Locate every leukocyte (white blood cell).
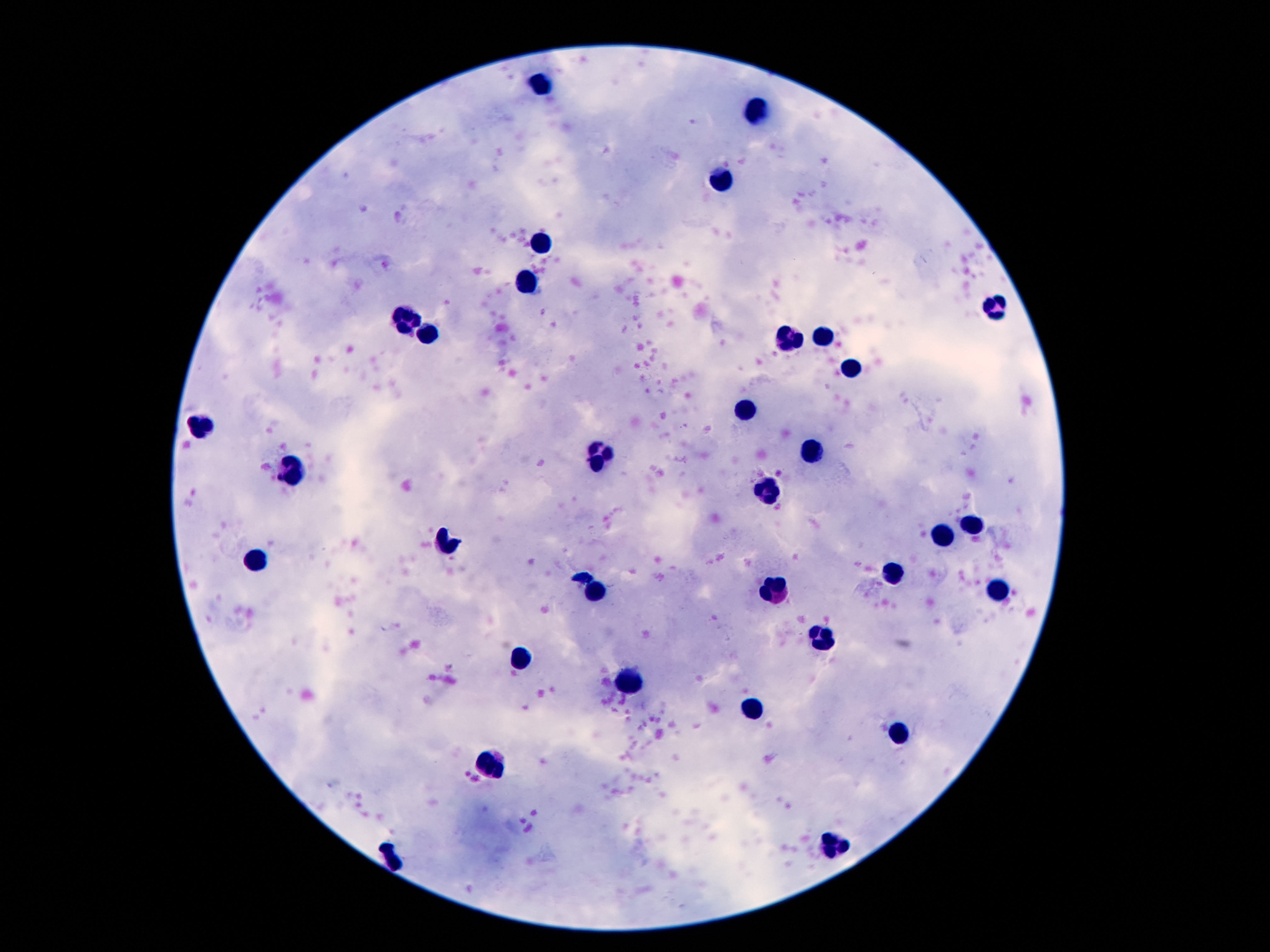

Approximate centers as {x, y} in pixels.
Leukocytes: {541, 82}, {758, 104}, {725, 175}, {539, 242}, {530, 283}, {993, 307}, {405, 321}, {425, 338}, {824, 338}, {789, 339}, {849, 367}, {749, 407}, {203, 427}, {814, 447}, {599, 458}, {292, 468}, {767, 493}, {973, 526}, {944, 537}, {446, 538}, {261, 559}, {893, 574}, {999, 592}, {599, 593}, {780, 593}, {820, 638}, {520, 658}, {626, 681}, {754, 708}, {897, 731}, {493, 766}, {833, 844}, {394, 859}.

image size = 1270×952 pixels
stain = Giemsa
capture = smartphone camera through the microscope eyepiece
field of view = one from this slide
preparation = thick peripheral-blood smear
patient malaria status = not infected
magnification = 100x